Locate and identify every blood parasite.
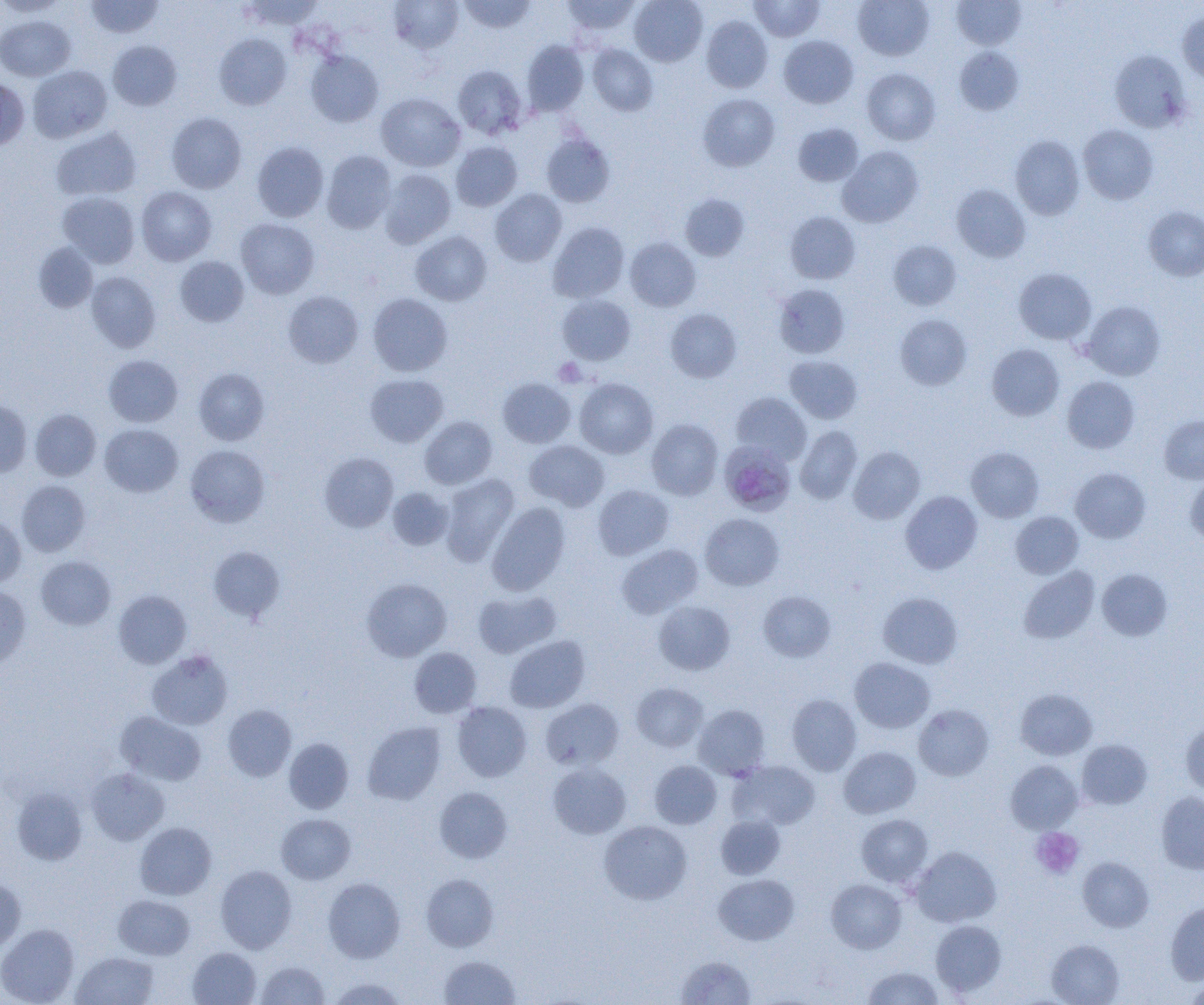

Approximate bounding boxes as named x1/y1/x2/y2 corners in pixels.
Plasmodium malariae-infected red blood cells: (x1=721, y1=440, x2=794, y2=514).
No Plasmodium falciparum, Plasmodium ovale, Plasmodium vivax, Babesia divergens, or Trypanosoma brucei observed.

Summary:
  - Uninfected red blood cell locations: (x1=85, y1=0, x2=163, y2=38), (x1=241, y1=0, x2=324, y2=30), (x1=388, y1=0, x2=463, y2=54), (x1=458, y1=0, x2=536, y2=33), (x1=561, y1=0, x2=641, y2=35), (x1=629, y1=0, x2=707, y2=66), (x1=749, y1=0, x2=824, y2=41), (x1=853, y1=0, x2=934, y2=60), (x1=0, y1=1, x2=68, y2=17), (x1=952, y1=1, x2=1025, y2=49), (x1=1178, y1=11, x2=1204, y2=85), (x1=0, y1=15, x2=75, y2=81), (x1=701, y1=15, x2=773, y2=93), (x1=214, y1=33, x2=291, y2=110), (x1=778, y1=35, x2=858, y2=108), (x1=521, y1=40, x2=589, y2=116), (x1=108, y1=41, x2=182, y2=111), (x1=588, y1=44, x2=658, y2=115), (x1=954, y1=47, x2=1024, y2=115), (x1=1109, y1=49, x2=1191, y2=133), (x1=306, y1=50, x2=383, y2=127), (x1=452, y1=64, x2=528, y2=139), (x1=27, y1=65, x2=112, y2=142), (x1=862, y1=68, x2=940, y2=145), (x1=0, y1=78, x2=29, y2=150), (x1=376, y1=93, x2=465, y2=171), (x1=698, y1=94, x2=779, y2=171), (x1=167, y1=112, x2=246, y2=193), (x1=793, y1=123, x2=864, y2=186), (x1=1078, y1=124, x2=1158, y2=204), (x1=51, y1=127, x2=141, y2=201), (x1=541, y1=133, x2=615, y2=207), (x1=1011, y1=135, x2=1085, y2=219), (x1=451, y1=141, x2=522, y2=211), (x1=252, y1=142, x2=329, y2=222), (x1=837, y1=146, x2=923, y2=227), (x1=322, y1=150, x2=397, y2=234), (x1=379, y1=169, x2=455, y2=248), (x1=951, y1=184, x2=1030, y2=262), (x1=137, y1=186, x2=216, y2=265), (x1=490, y1=189, x2=567, y2=266), (x1=58, y1=192, x2=140, y2=268), (x1=680, y1=194, x2=749, y2=261), (x1=1143, y1=206, x2=1204, y2=280), (x1=785, y1=211, x2=861, y2=284), (x1=236, y1=218, x2=320, y2=299), (x1=548, y1=222, x2=629, y2=303), (x1=411, y1=231, x2=491, y2=306), (x1=625, y1=238, x2=701, y2=311), (x1=888, y1=240, x2=961, y2=310), (x1=33, y1=242, x2=98, y2=313), (x1=175, y1=256, x2=248, y2=326), (x1=1014, y1=268, x2=1096, y2=344), (x1=86, y1=272, x2=161, y2=352), (x1=774, y1=284, x2=850, y2=358), (x1=283, y1=291, x2=363, y2=368), (x1=368, y1=293, x2=452, y2=376), (x1=557, y1=294, x2=635, y2=365), (x1=1080, y1=301, x2=1165, y2=380), (x1=665, y1=308, x2=741, y2=382), (x1=895, y1=314, x2=971, y2=389), (x1=987, y1=344, x2=1064, y2=420), (x1=104, y1=355, x2=183, y2=427), (x1=784, y1=355, x2=862, y2=424), (x1=194, y1=368, x2=270, y2=445), (x1=365, y1=374, x2=448, y2=447), (x1=1062, y1=376, x2=1140, y2=453), (x1=497, y1=378, x2=575, y2=448), (x1=574, y1=378, x2=658, y2=459), (x1=731, y1=392, x2=812, y2=464), (x1=0, y1=400, x2=32, y2=477), (x1=30, y1=409, x2=101, y2=480), (x1=1159, y1=415, x2=1204, y2=483), (x1=419, y1=416, x2=497, y2=489), (x1=647, y1=419, x2=723, y2=500), (x1=100, y1=424, x2=183, y2=497), (x1=795, y1=426, x2=862, y2=504), (x1=524, y1=440, x2=609, y2=511), (x1=185, y1=445, x2=270, y2=527), (x1=848, y1=446, x2=925, y2=524), (x1=966, y1=447, x2=1044, y2=522), (x1=319, y1=452, x2=398, y2=532), (x1=1070, y1=467, x2=1150, y2=543), (x1=441, y1=474, x2=519, y2=564), (x1=1185, y1=476, x2=1204, y2=546), (x1=17, y1=480, x2=90, y2=556), (x1=593, y1=485, x2=674, y2=560), (x1=387, y1=487, x2=453, y2=550), (x1=900, y1=491, x2=982, y2=574), (x1=486, y1=502, x2=570, y2=595), (x1=1010, y1=511, x2=1083, y2=578), (x1=700, y1=512, x2=784, y2=590), (x1=0, y1=516, x2=26, y2=588), (x1=617, y1=544, x2=703, y2=618), (x1=207, y1=546, x2=285, y2=622), (x1=36, y1=556, x2=115, y2=629), (x1=1019, y1=566, x2=1100, y2=644), (x1=1097, y1=568, x2=1172, y2=640), (x1=362, y1=578, x2=452, y2=661), (x1=0, y1=586, x2=31, y2=671), (x1=473, y1=589, x2=560, y2=658), (x1=113, y1=590, x2=191, y2=668), (x1=758, y1=591, x2=835, y2=662), (x1=878, y1=593, x2=963, y2=668), (x1=654, y1=601, x2=734, y2=675), (x1=505, y1=635, x2=590, y2=713), (x1=409, y1=647, x2=481, y2=718), (x1=147, y1=650, x2=233, y2=730), (x1=849, y1=657, x2=935, y2=733), (x1=631, y1=682, x2=708, y2=752), (x1=1015, y1=689, x2=1097, y2=760), (x1=786, y1=694, x2=861, y2=775), (x1=540, y1=698, x2=624, y2=770), (x1=452, y1=701, x2=532, y2=782), (x1=223, y1=705, x2=296, y2=781), (x1=693, y1=705, x2=771, y2=778), (x1=914, y1=705, x2=994, y2=780), (x1=116, y1=711, x2=205, y2=785), (x1=1181, y1=720, x2=1204, y2=797), (x1=362, y1=721, x2=446, y2=805), (x1=284, y1=737, x2=354, y2=813), (x1=1077, y1=739, x2=1151, y2=810), (x1=839, y1=746, x2=920, y2=818), (x1=649, y1=760, x2=722, y2=829), (x1=730, y1=760, x2=820, y2=830), (x1=1005, y1=760, x2=1083, y2=834), (x1=548, y1=763, x2=631, y2=839), (x1=86, y1=768, x2=169, y2=845), (x1=12, y1=787, x2=87, y2=865), (x1=434, y1=787, x2=513, y2=863), (x1=1156, y1=791, x2=1204, y2=874), (x1=276, y1=813, x2=355, y2=884), (x1=856, y1=814, x2=933, y2=887), (x1=715, y1=815, x2=785, y2=879), (x1=599, y1=821, x2=692, y2=904), (x1=135, y1=822, x2=216, y2=900), (x1=910, y1=846, x2=1001, y2=927), (x1=1077, y1=857, x2=1154, y2=932), (x1=215, y1=865, x2=297, y2=953), (x1=421, y1=874, x2=499, y2=952), (x1=714, y1=874, x2=799, y2=945), (x1=0, y1=877, x2=26, y2=952), (x1=323, y1=877, x2=405, y2=963), (x1=826, y1=878, x2=906, y2=953), (x1=113, y1=894, x2=195, y2=960), (x1=1166, y1=902, x2=1204, y2=985), (x1=930, y1=920, x2=1006, y2=997), (x1=0, y1=923, x2=79, y2=1005), (x1=1047, y1=939, x2=1124, y2=1005), (x1=187, y1=947, x2=261, y2=1005), (x1=72, y1=952, x2=158, y2=1005), (x1=440, y1=955, x2=520, y2=1004), (x1=675, y1=955, x2=756, y2=1004), (x1=255, y1=961, x2=329, y2=1005), (x1=862, y1=966, x2=944, y2=1005), (x1=328, y1=977, x2=407, y2=1005), (x1=1184, y1=977, x2=1204, y2=1004)
  - Platelet locations: (x1=553, y1=358, x2=587, y2=387), (x1=1031, y1=827, x2=1085, y2=879)
  - Slide-level diagnosis: Plasmodium malariae
  - Field of view: single
  - Image size: 1204×1005 pixels
  - Modality: optical microscopy
  - Magnification: 1000x
  - Preparation: thin blood smear